Locate and identify every blood parasite.
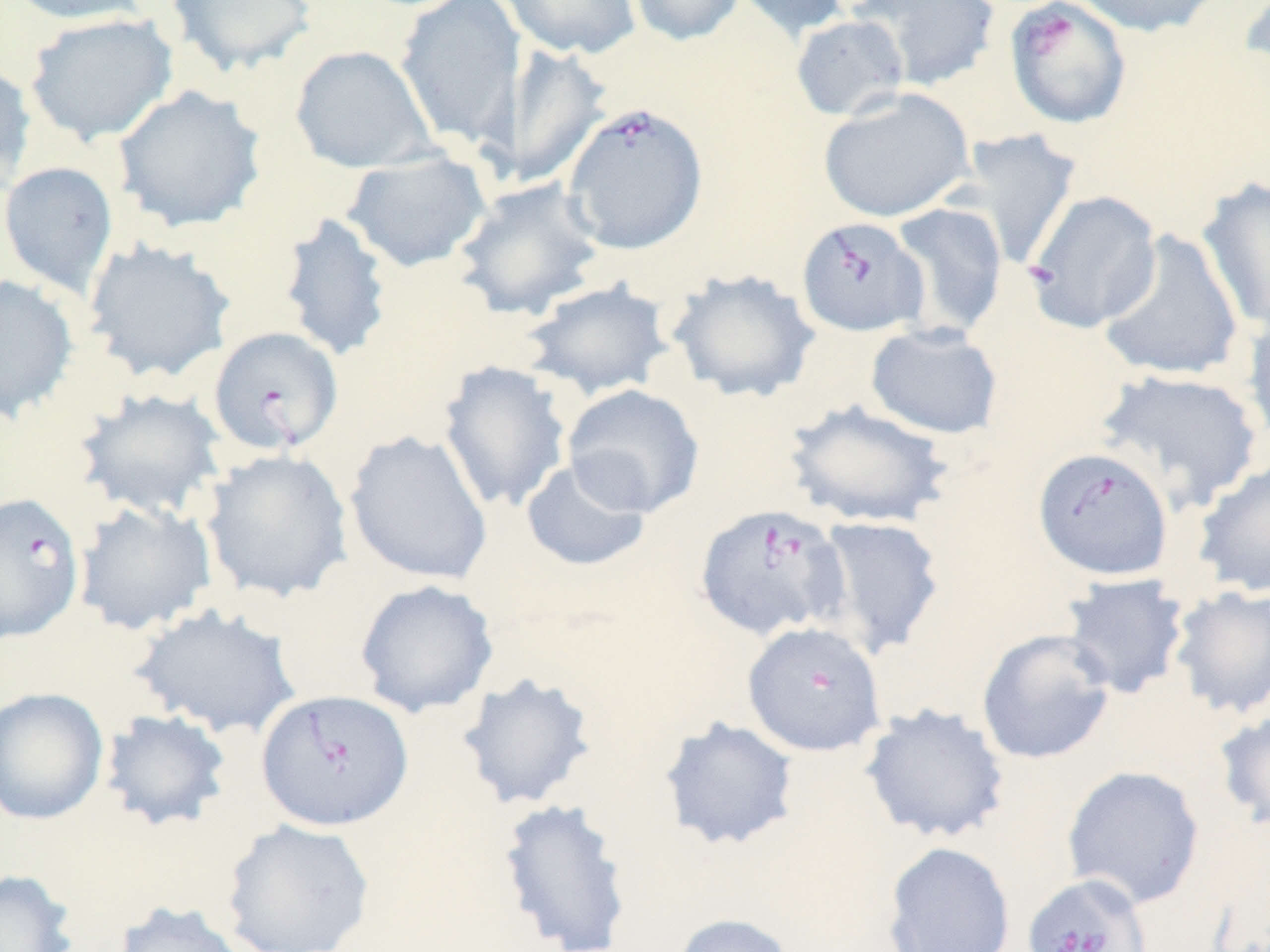
Approximate bounding boxes as named x1/y1/x2/y2 corners in pixels.
Babesia divergens-infected red blood cells: (x1=1003, y1=0, x2=1134, y2=130), (x1=561, y1=101, x2=709, y2=255), (x1=1022, y1=189, x2=1163, y2=334), (x1=796, y1=215, x2=929, y2=338), (x1=208, y1=325, x2=344, y2=456), (x1=1033, y1=445, x2=1174, y2=580), (x1=0, y1=491, x2=85, y2=645), (x1=693, y1=502, x2=849, y2=641), (x1=741, y1=621, x2=887, y2=757), (x1=255, y1=689, x2=414, y2=830), (x1=1021, y1=872, x2=1153, y2=952).
No Plasmodium falciparum, Plasmodium ovale, Plasmodium malariae, Plasmodium vivax, or Trypanosoma brucei observed.

Summary:
  - Uninfected red blood cell locations: (x1=6, y1=0, x2=151, y2=25), (x1=165, y1=0, x2=318, y2=77), (x1=394, y1=0, x2=527, y2=150), (x1=499, y1=0, x2=642, y2=60), (x1=625, y1=0, x2=749, y2=47), (x1=729, y1=0, x2=854, y2=42), (x1=847, y1=0, x2=1002, y2=91), (x1=1068, y1=0, x2=1227, y2=38), (x1=1238, y1=0, x2=1270, y2=89), (x1=23, y1=12, x2=178, y2=146), (x1=789, y1=14, x2=911, y2=122), (x1=493, y1=42, x2=614, y2=191), (x1=289, y1=44, x2=438, y2=174), (x1=0, y1=60, x2=37, y2=195), (x1=112, y1=84, x2=268, y2=234), (x1=817, y1=87, x2=975, y2=223), (x1=947, y1=127, x2=1082, y2=270), (x1=341, y1=149, x2=492, y2=273), (x1=0, y1=161, x2=119, y2=298), (x1=1196, y1=176, x2=1270, y2=333), (x1=451, y1=177, x2=607, y2=322), (x1=888, y1=202, x2=1009, y2=340), (x1=277, y1=211, x2=395, y2=363), (x1=1097, y1=229, x2=1245, y2=382), (x1=82, y1=238, x2=237, y2=385), (x1=665, y1=268, x2=821, y2=404), (x1=0, y1=273, x2=80, y2=424), (x1=520, y1=279, x2=676, y2=401), (x1=1241, y1=306, x2=1270, y2=454), (x1=864, y1=323, x2=1005, y2=440), (x1=436, y1=360, x2=572, y2=514), (x1=1094, y1=367, x2=1265, y2=514), (x1=562, y1=384, x2=705, y2=518), (x1=73, y1=387, x2=229, y2=521), (x1=782, y1=398, x2=956, y2=529), (x1=344, y1=428, x2=494, y2=586), (x1=200, y1=449, x2=353, y2=603), (x1=520, y1=457, x2=652, y2=573), (x1=1192, y1=457, x2=1270, y2=598), (x1=73, y1=500, x2=218, y2=636), (x1=812, y1=515, x2=947, y2=659), (x1=1059, y1=572, x2=1191, y2=700), (x1=354, y1=579, x2=499, y2=718), (x1=1167, y1=585, x2=1270, y2=720), (x1=130, y1=603, x2=302, y2=740), (x1=976, y1=629, x2=1117, y2=765), (x1=455, y1=670, x2=599, y2=812), (x1=0, y1=687, x2=109, y2=825), (x1=859, y1=702, x2=1011, y2=844), (x1=99, y1=708, x2=233, y2=832), (x1=1213, y1=709, x2=1270, y2=832), (x1=658, y1=715, x2=801, y2=852), (x1=1061, y1=765, x2=1206, y2=909), (x1=497, y1=797, x2=634, y2=952), (x1=220, y1=818, x2=376, y2=952), (x1=882, y1=841, x2=1016, y2=951), (x1=0, y1=867, x2=80, y2=952), (x1=112, y1=899, x2=250, y2=952), (x1=670, y1=912, x2=797, y2=952)
  - Slide-level diagnosis: Babesia divergens
  - Magnification: 1000x
  - Field of view: one of a larger specimen
  - Image size: 1270×952 pixels
  - Modality: optical microscopy
  - Stain: May-Grünwald-Giemsa
  - Preparation: thin blood smear